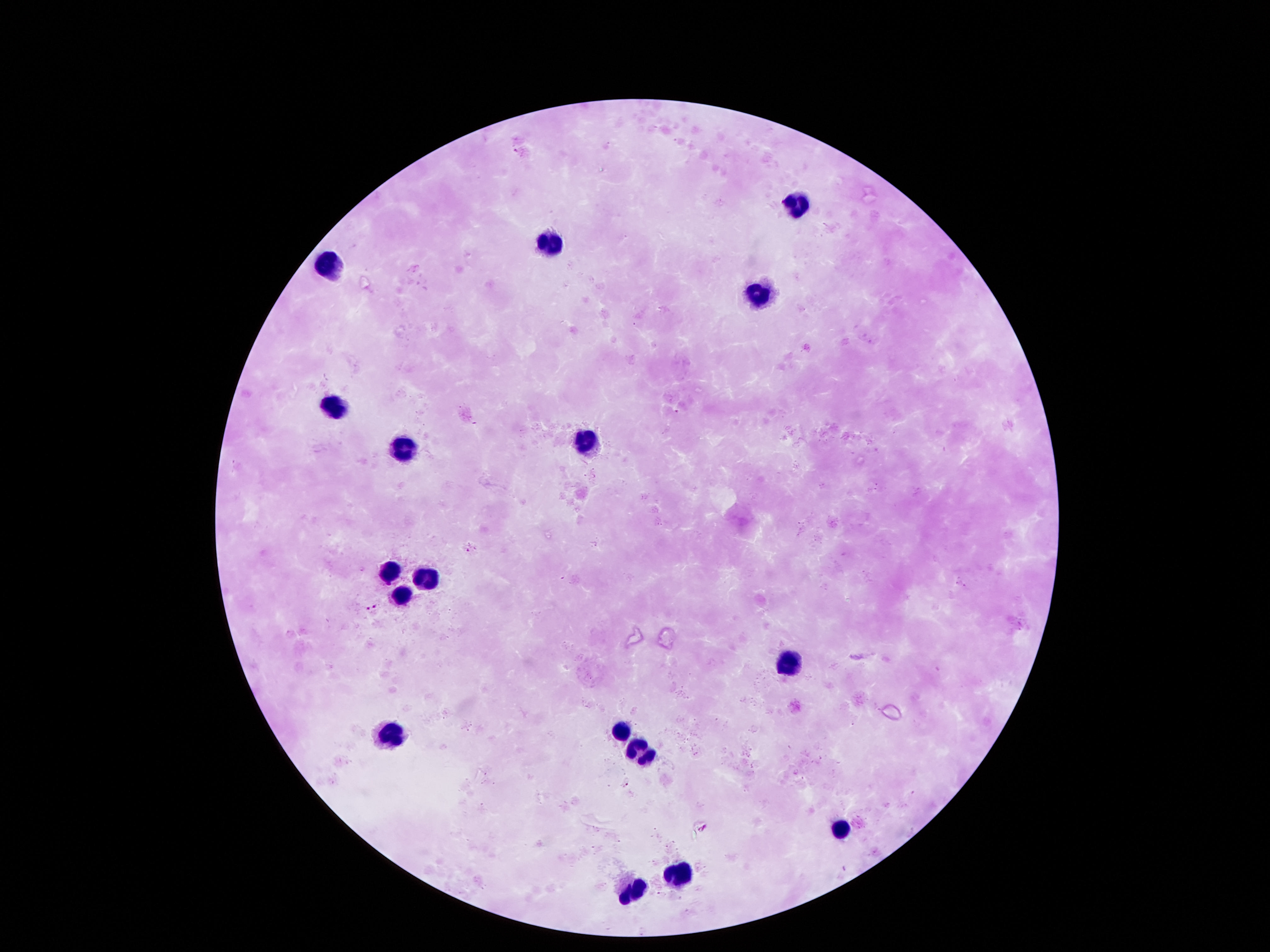
Approximate centers as [x, y] in pixels.
Summary:
  - Leukocyte locations: [797, 200], [551, 234], [333, 264], [756, 297], [329, 408], [585, 436], [400, 442], [387, 572], [424, 576], [400, 590], [787, 664], [390, 728], [619, 731], [639, 751], [844, 825], [679, 869], [622, 891]
  - Stain: Giemsa
  - Capture: smartphone camera through the microscope eyepiece
  - Patient malaria status: negative
  - Field of view: one from this slide
  - Image size: 1270×952 pixels
  - Magnification: 100x
  - Preparation: thick peripheral-blood smear